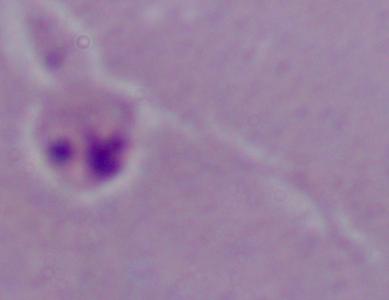

modality = micrograph
magnification = 1000x
identification = Leishmania